Point out each Plasmodium parasite.
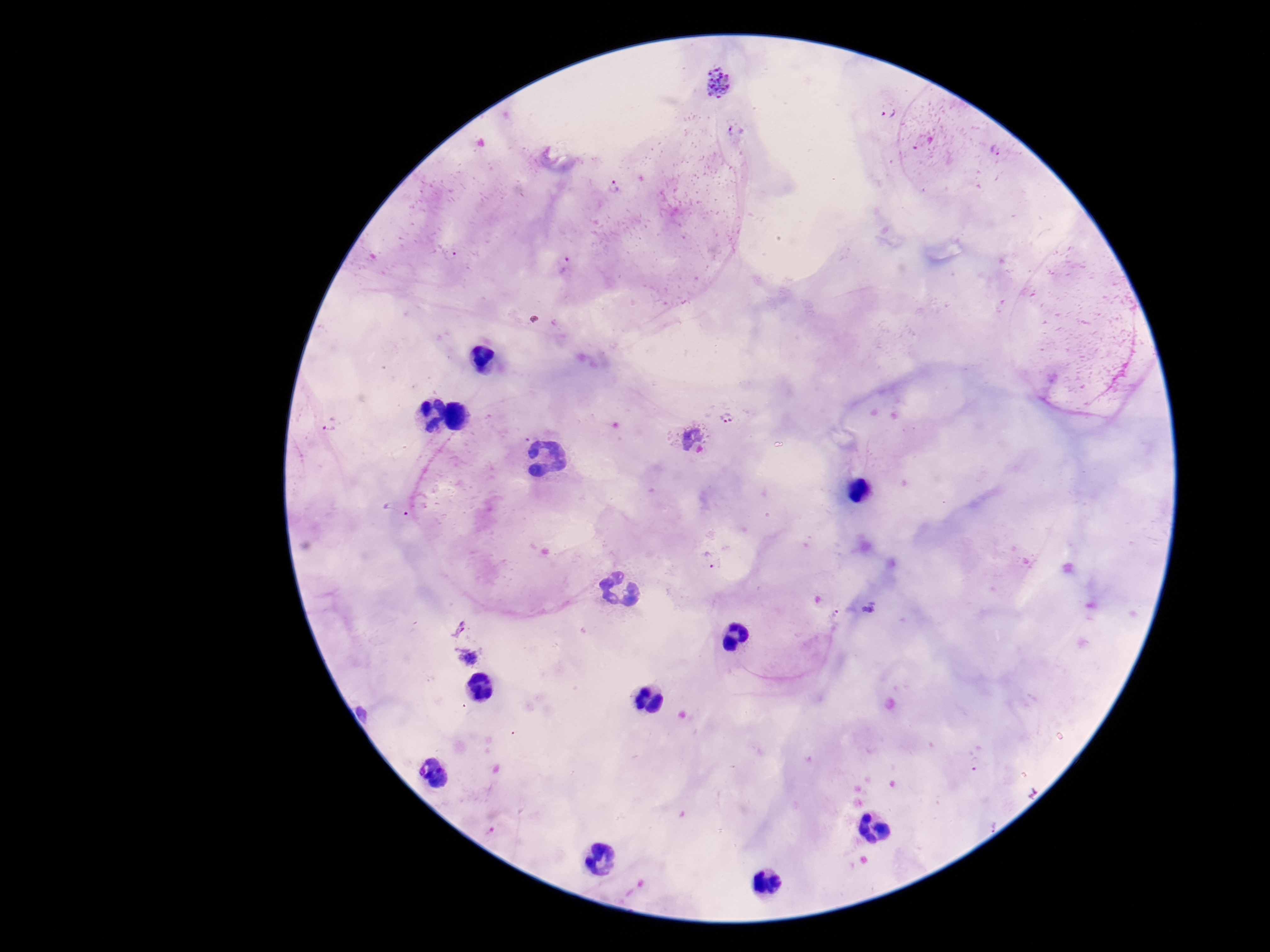
Approximate centers as {x, y} in pixels.
Plasmodium parasites: {718, 82}, {889, 111}, {737, 128}, {995, 150}, {613, 186}, {564, 265}, {731, 415}, {331, 425}, {688, 439}, {398, 509}, {711, 558}, {836, 615}, {460, 627}.

Giemsa stain. Photographed through the microscope eyepiece with a smartphone camera. Thick blood film. Image is 1270×952 pixels. 100x magnification. Patient malaria status: positive. One field from this slide.